State which cell type is depicted.
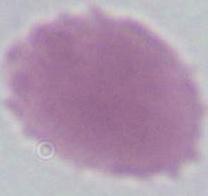

An erythrocyte.

magnification: 1000x
modality: photomicrograph